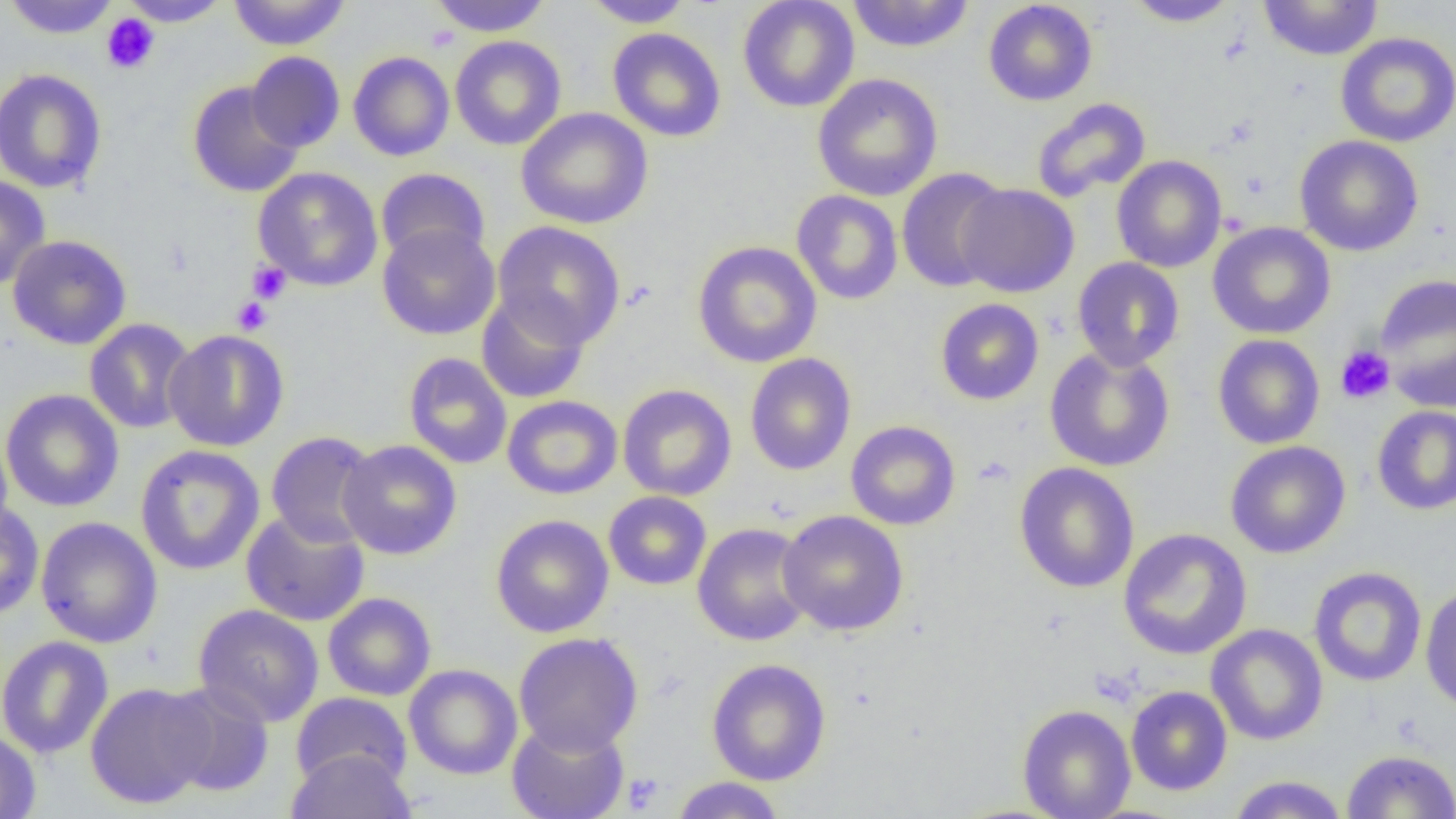 Approximate bounding boxes as (x1,y1)-(x2,y2) corner pairs in pixels. Platelet locations: (101,13)-(160,74), (247,261)-(291,304), (232,296)-(272,334), (1336,345)-(1395,404), (622,772)-(665,812). Uninfected red blood cell locations: (2,0)-(121,39), (118,0)-(231,27), (228,0)-(351,50), (428,0)-(552,37), (580,0)-(695,28), (737,0)-(859,112), (1125,0)-(1240,27), (1258,0)-(1383,61), (846,1)-(974,52), (982,1)-(1098,106), (607,27)-(726,142), (1335,32)-(1456,148), (450,35)-(566,150), (246,51)-(345,152), (348,51)-(454,161), (0,68)-(107,195), (812,73)-(943,201), (187,80)-(303,198), (1031,97)-(1151,203), (516,107)-(653,230), (1295,135)-(1424,256), (1111,156)-(1226,272), (253,167)-(383,291), (375,167)-(491,266), (895,167)-(1011,293), (0,176)-(51,289), (956,183)-(1080,298), (791,190)-(903,305), (492,221)-(626,349), (1207,222)-(1336,340), (377,223)-(500,340), (7,235)-(132,350), (692,240)-(822,368), (1071,257)-(1185,371), (1375,273)-(1456,412), (476,292)-(591,403), (935,298)-(1044,405), (84,318)-(198,434), (163,329)-(290,452), (1212,334)-(1325,449), (1044,346)-(1175,473), (403,352)-(513,469), (744,353)-(856,476), (617,384)-(736,501), (1,389)-(124,512), (502,395)-(622,500), (1371,405)-(1456,515), (845,420)-(961,530), (0,426)-(13,539), (266,431)-(381,548), (338,440)-(462,560), (1225,441)-(1351,558), (135,445)-(266,576), (1014,462)-(1140,593), (603,491)-(712,591), (0,502)-(45,619), (777,509)-(909,636), (240,510)-(370,627), (490,514)-(614,638), (36,517)-(162,648), (693,522)-(814,646), (1118,528)-(1252,660), (1309,567)-(1427,688), (1420,584)-(1456,712), (323,592)-(436,701), (193,604)-(324,727), (1206,624)-(1328,745), (513,632)-(643,756), (0,636)-(114,758), (706,658)-(831,785), (404,664)-(522,780), (157,681)-(275,798), (85,682)-(215,809), (1126,686)-(1232,796), (290,692)-(413,790), (1016,704)-(1136,819), (507,719)-(630,819), (0,728)-(41,819), (287,747)-(416,819), (1341,749)-(1456,818), (1226,775)-(1351,818), (670,777)-(787,818). Slide-level diagnosis: no evidence of blood parasites. 1000x magnification. Light microscopy. Image is 1456×819 pixels. One field of a larger specimen. Thin blood film.